Locate every Plasmodium parasite.
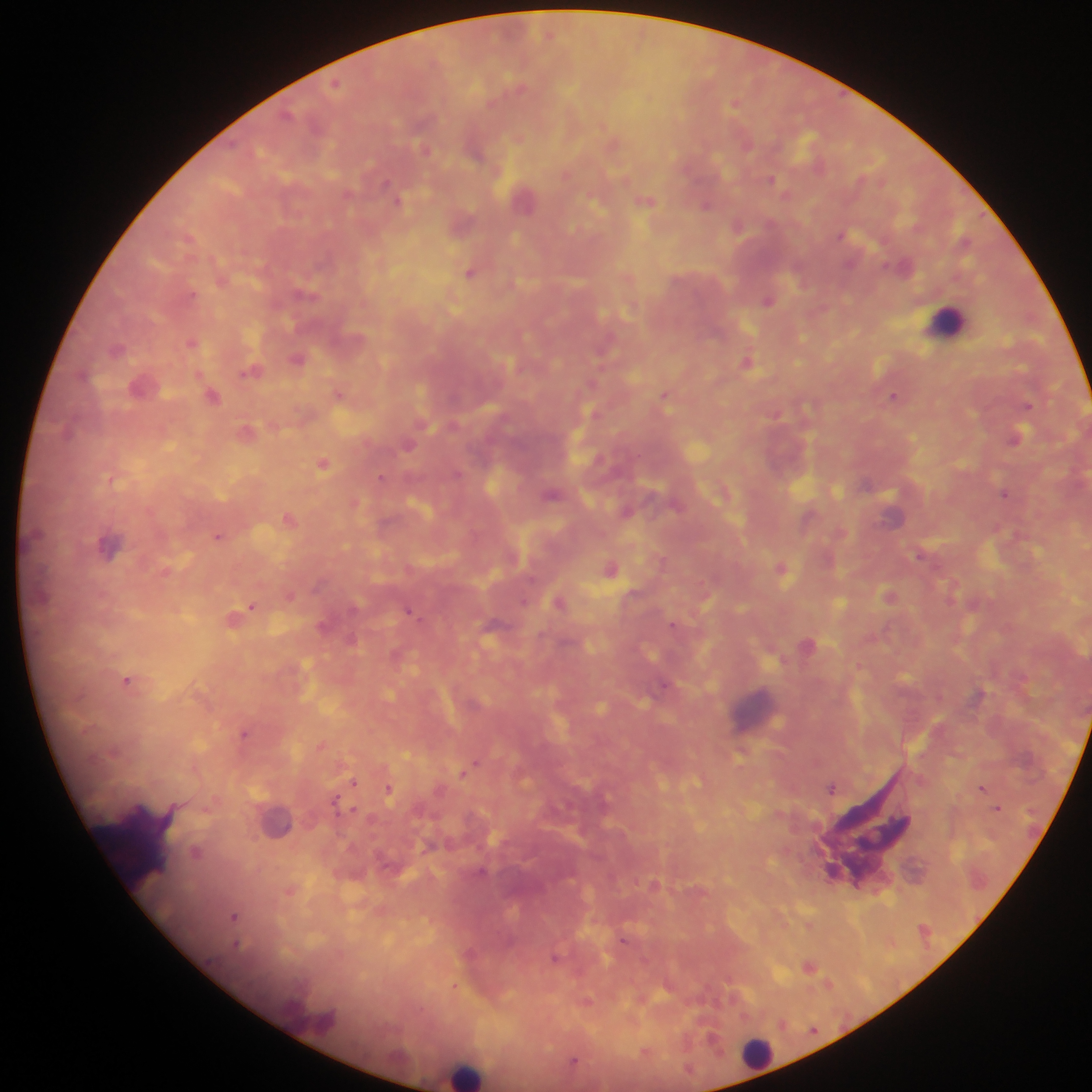

Approximate centers as x y in pixels.
Plasmodium parasites: 337 82; 735 104; 771 178; 385 182; 347 192; 786 194; 399 199; 738 225; 841 235; 470 272; 192 296; 768 301; 189 341; 296 359; 747 361; 250 372; 339 392; 664 394; 895 396; 1028 405; 1017 438; 409 447; 323 463; 381 477; 112 481; 1006 495; 290 518; 219 537; 661 559; 611 568; 783 568; 702 584; 890 593; 290 595; 559 601; 252 606; 408 609; 244 611; 673 623; 807 645; 860 664; 127 679; 1022 679; 664 683; 245 733; 322 746; 478 761; 461 774; 354 782; 983 787; 833 788; 390 789; 335 799; 355 809; 207 810; 196 851; 656 883; 290 892; 235 917; 810 966; 453 985; 586 1000.

country: Ghana
leukocyte_locations: 'approximate centers as x y in pixels: 942 327; 756 1056; 463 1077'
capture: mobile-phone photograph through a microscope
image_size: 1092×1092 pixels
preparation: thick blood film
field_of_view: single